Outline each uninfected red blood cell.
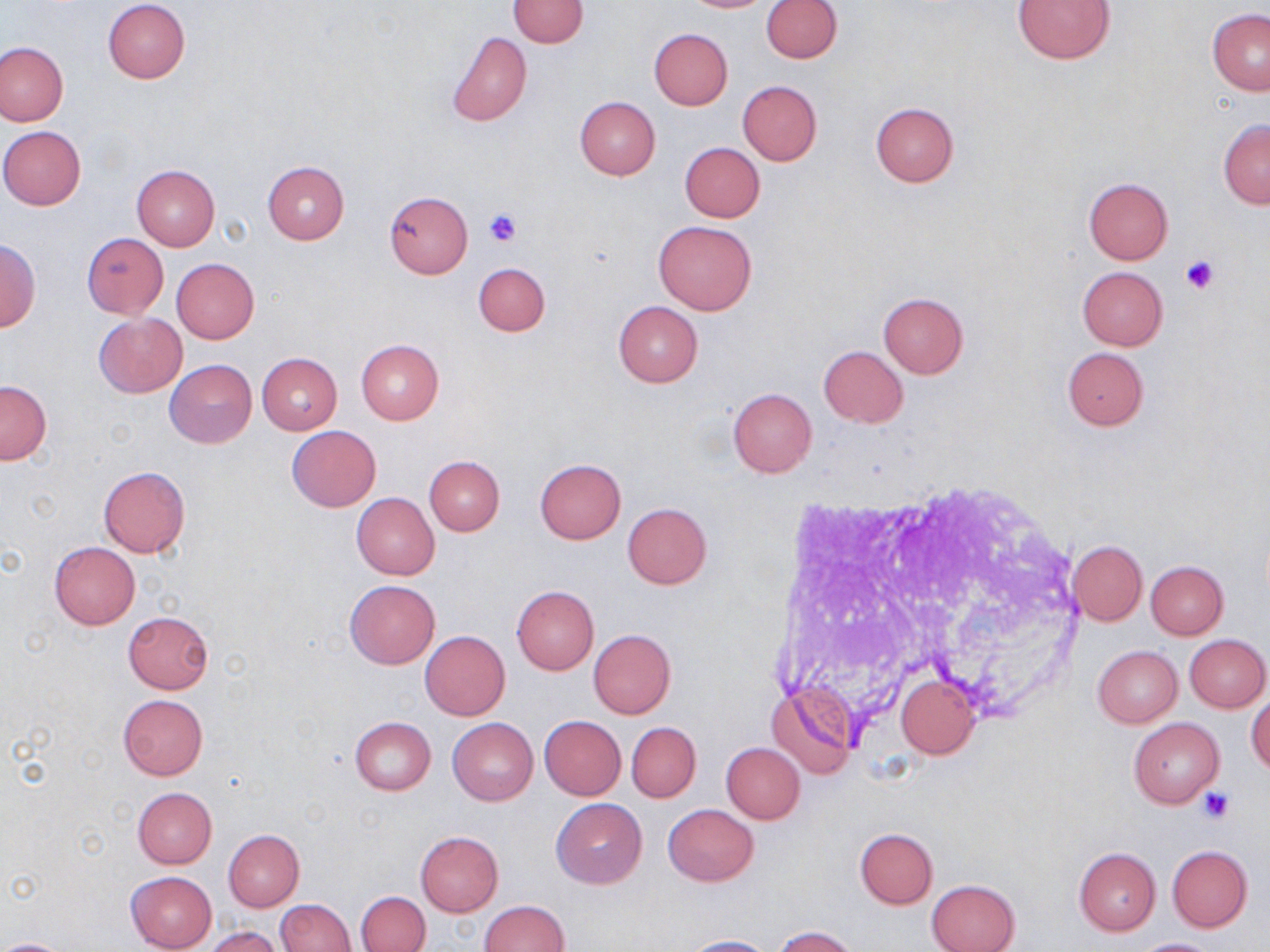

Approximate bounding boxes as (x1, y1, x2, y2) in pixels.
Uninfected red blood cells: (102, 0, 190, 84), (508, 0, 588, 48), (681, 0, 773, 12), (760, 0, 842, 62), (1013, 0, 1116, 64), (1207, 9, 1270, 95), (649, 28, 733, 109), (447, 33, 533, 127), (0, 42, 67, 126), (738, 81, 823, 165), (574, 97, 660, 180), (870, 103, 959, 188), (1218, 118, 1270, 208), (0, 126, 87, 210), (680, 142, 764, 223), (262, 160, 349, 244), (132, 164, 220, 250), (1083, 177, 1173, 264), (384, 191, 473, 277), (652, 221, 757, 315), (81, 233, 169, 318), (0, 240, 42, 331), (172, 258, 259, 343), (474, 262, 550, 336), (1077, 266, 1168, 350), (878, 293, 967, 379), (612, 300, 703, 387), (94, 313, 186, 397), (356, 339, 444, 423), (818, 345, 908, 428), (1062, 347, 1149, 430), (257, 352, 343, 434), (165, 360, 257, 448), (0, 380, 51, 463), (728, 388, 817, 477), (286, 426, 382, 512), (424, 456, 505, 536), (535, 459, 626, 544), (98, 466, 190, 557), (351, 493, 440, 579), (623, 503, 712, 589), (1068, 540, 1147, 625), (49, 541, 140, 629), (1145, 560, 1228, 639), (345, 579, 439, 668), (512, 586, 599, 675), (123, 611, 214, 695), (588, 630, 676, 719), (420, 631, 510, 721), (1185, 633, 1268, 712), (1092, 646, 1183, 727), (895, 674, 981, 759), (769, 686, 857, 781), (1247, 691, 1270, 777), (118, 694, 207, 780), (539, 716, 625, 799), (350, 717, 435, 795), (448, 718, 538, 804), (1128, 718, 1223, 807), (626, 722, 700, 803), (722, 743, 805, 824), (132, 787, 217, 868), (552, 799, 646, 889), (663, 804, 759, 886), (855, 828, 938, 908), (224, 830, 304, 911), (415, 831, 503, 915), (1167, 845, 1252, 931), (1073, 847, 1160, 936), (125, 871, 217, 952), (927, 879, 1019, 952), (357, 891, 430, 952), (275, 899, 355, 951), (478, 900, 569, 952), (772, 926, 859, 952), (204, 927, 283, 952), (679, 935, 773, 952), (1131, 937, 1223, 951), (0, 939, 69, 952).

Summary:
  - Platelet locations: (483, 207, 523, 246), (1182, 256, 1222, 294), (1200, 788, 1234, 822)
  - Slide-level diagnosis: negative for blood parasites
  - Image size: 1270×952 pixels
  - Preparation: thin blood film
  - Magnification: 1000x
  - Field of view: single
  - Modality: optical microscopy
  - Stain: May-Grünwald-Giemsa